Assess this cell for malaria.
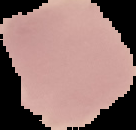

It is uninfected.

Summary:
  - Preparation: thin blood film
  - Image type: cell region segmented out of the field of view; surrounding area masked to black
  - Image size: 136×130 pixels